Comment on the morphology of the erythrocytes.
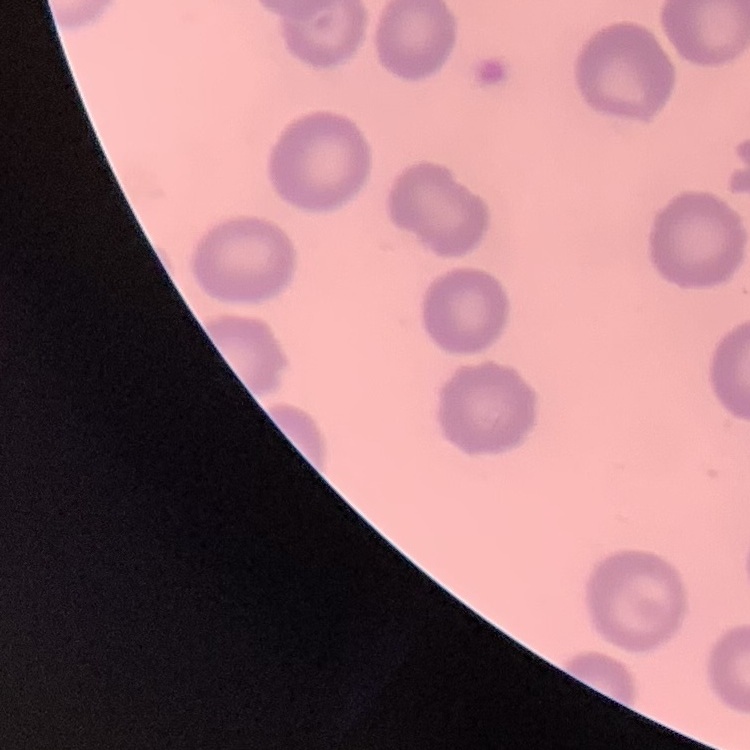

They show no rouleaux formation.

Summary:
  - Stain: Field's or Giemsa
  - Preparation: thin blood film
  - Image type: square crop of a larger photomicrograph